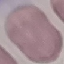

Summary:
  - Result: no malaria parasites detected
  - Image type: automatically extracted cell patch, resized to 64 × 64 pixels
  - Capture: smartphone through the microscope eyepiece
  - Preparation: thin smear
  - Stain: Giemsa